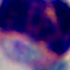
modality = micrograph
magnification = 1000x
identification = white blood cell